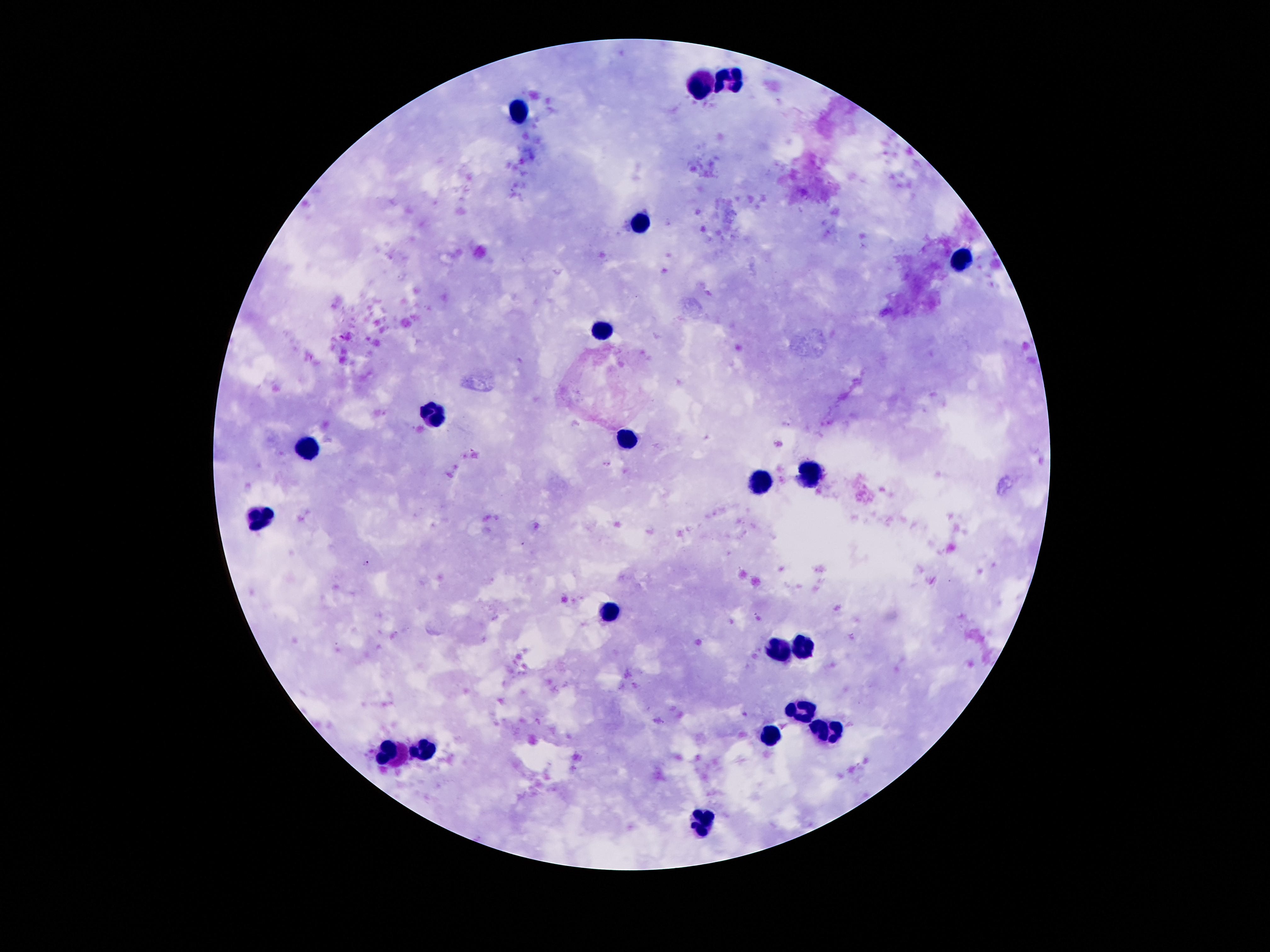
Approximate centers as (x, y) in pixels. Leukocyte locations: (730, 79), (698, 84), (519, 110), (640, 226), (962, 261), (604, 329), (433, 414), (628, 439), (305, 447), (809, 474), (757, 483), (258, 521), (609, 611), (777, 648), (801, 650), (804, 709), (826, 732), (771, 737), (426, 747), (396, 756), (700, 823). Giemsa-stained preparation. 100x magnification. Thick blood smear. Patient malaria status: not infected. Photographed through the microscope eyepiece with a smartphone camera. Image is 1270×952 pixels. One field from this slide.